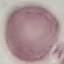

{
  "result": "negative for malaria parasites",
  "capture": "smartphone through the microscope eyepiece",
  "preparation": "thin smear",
  "image_type": "automatically extracted cell patch, resized to 64 × 64 pixels",
  "stain": "Giemsa"
}